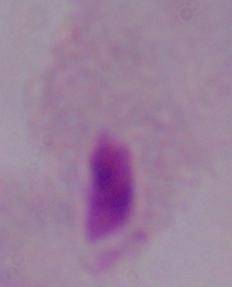

modality = micrograph
magnification = 1000x
identification = trichomonad